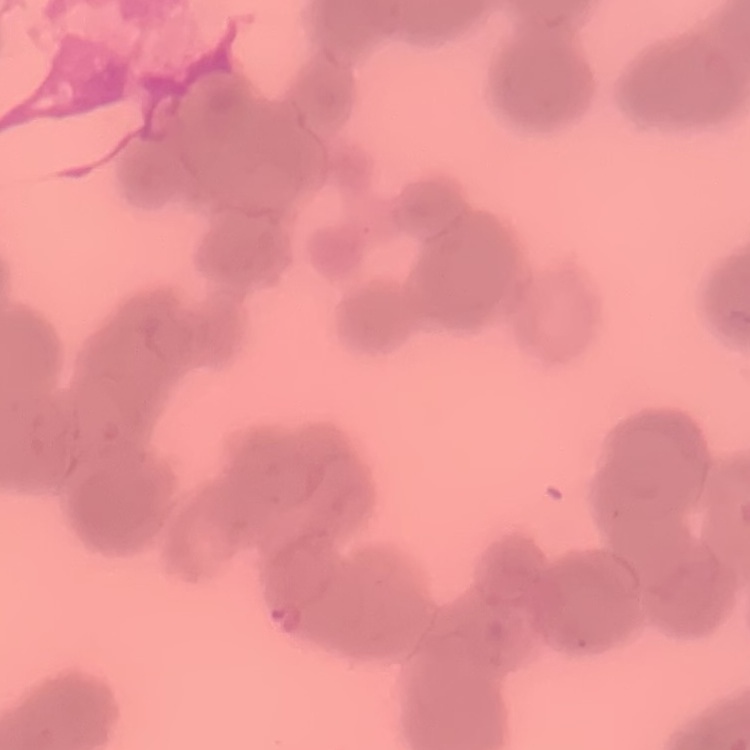

Summary:
  - Erythrocyte morphology: rouleaux formation
  - Preparation: thin peripheral smear
  - Stain: Field's or Giemsa
  - Image type: one tile cut from a larger photomicrograph